Report the malaria status.
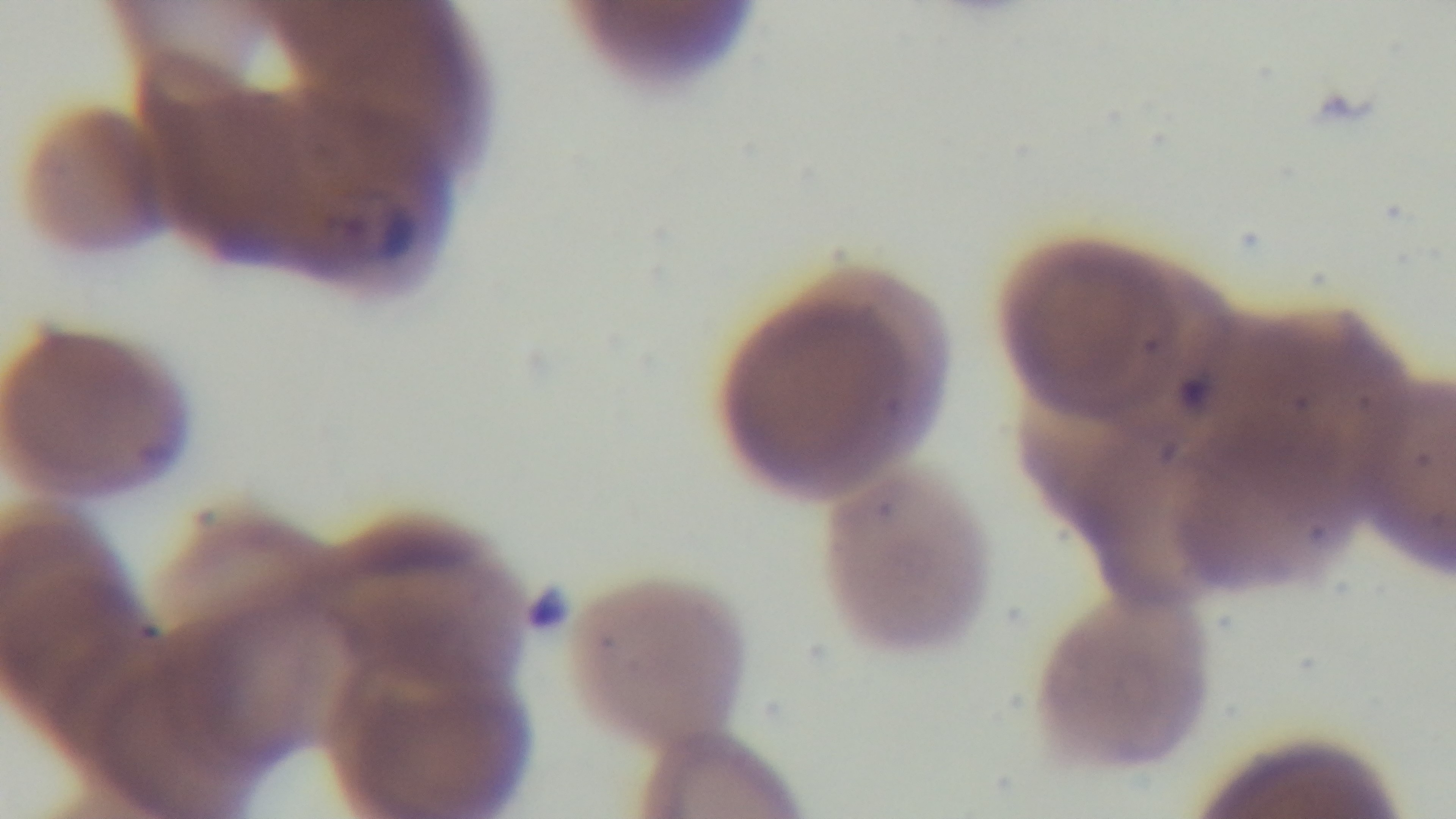

Positive.

field of view = single
modality = light microscopy
preparation = thin blood film
objective = 100x oil immersion
stain = Giemsa
capture = mounted 4K digital camera